Evaluate for Plasmodium parasites.
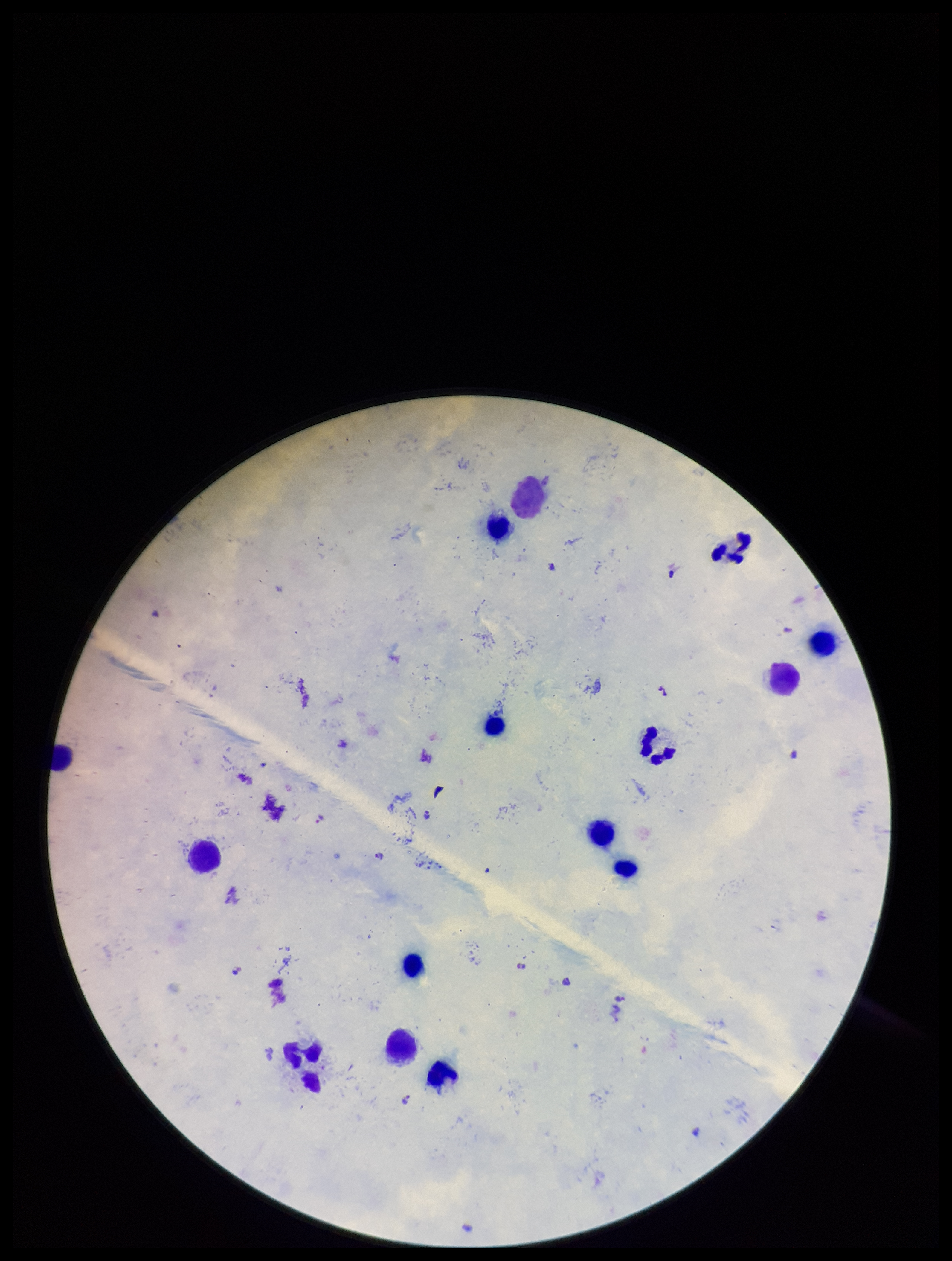

Seen.

leukocyte_count: 14
parasite_count: 8
species_reported_for_this_patient: Plasmodium falciparum
stain: Giemsa
field_of_view: single
image_size: 952×1261 pixels
capture: smartphone photograph through the microscope eyepiece
preparation: thick smear
patient_malaria_status: positive